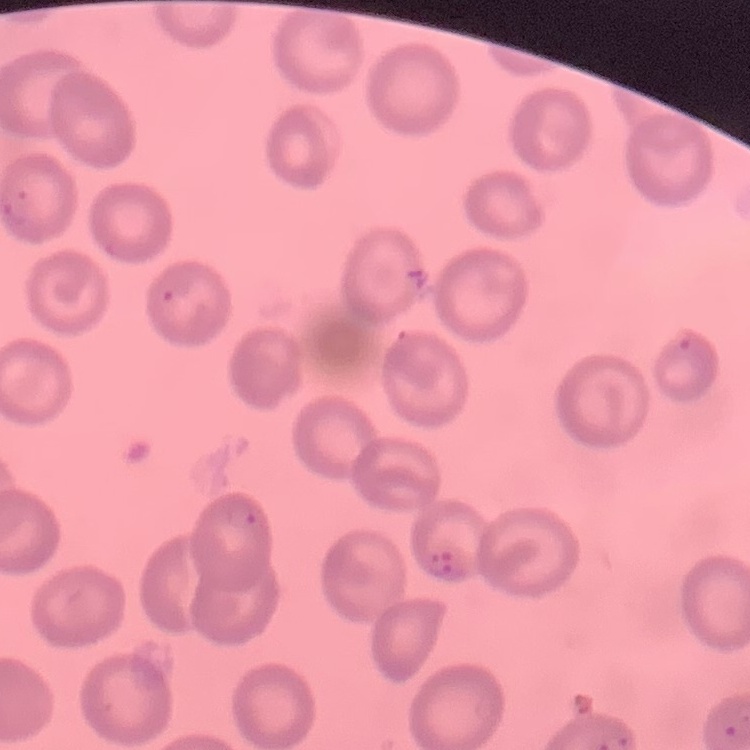

Summary:
  - Red blood cell morphology: no rouleaux formation
  - Image type: square crop of a larger photomicrograph
  - Preparation: thin blood smear
  - Stain: Field's or Giemsa